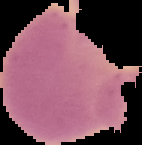
{
  "preparation": "thin blood smear",
  "result": "negative for malaria parasites",
  "image_size": "142×145 pixels",
  "image_type": "cell region segmented out of the field of view; surrounding area masked to black"
}